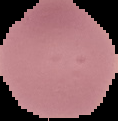

image size = 118×121 pixels
preparation = thin blood smear
malaria status = uninfected
image type = segmented cell region with the area outside set to black